Name the parasite shown.
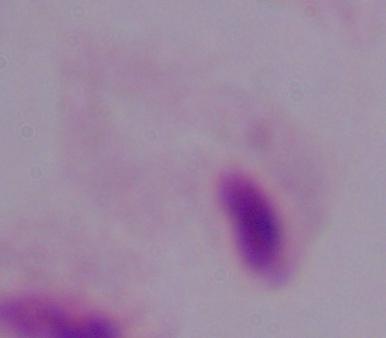
A trichomonad.

magnification = 1000x
modality = photomicrograph